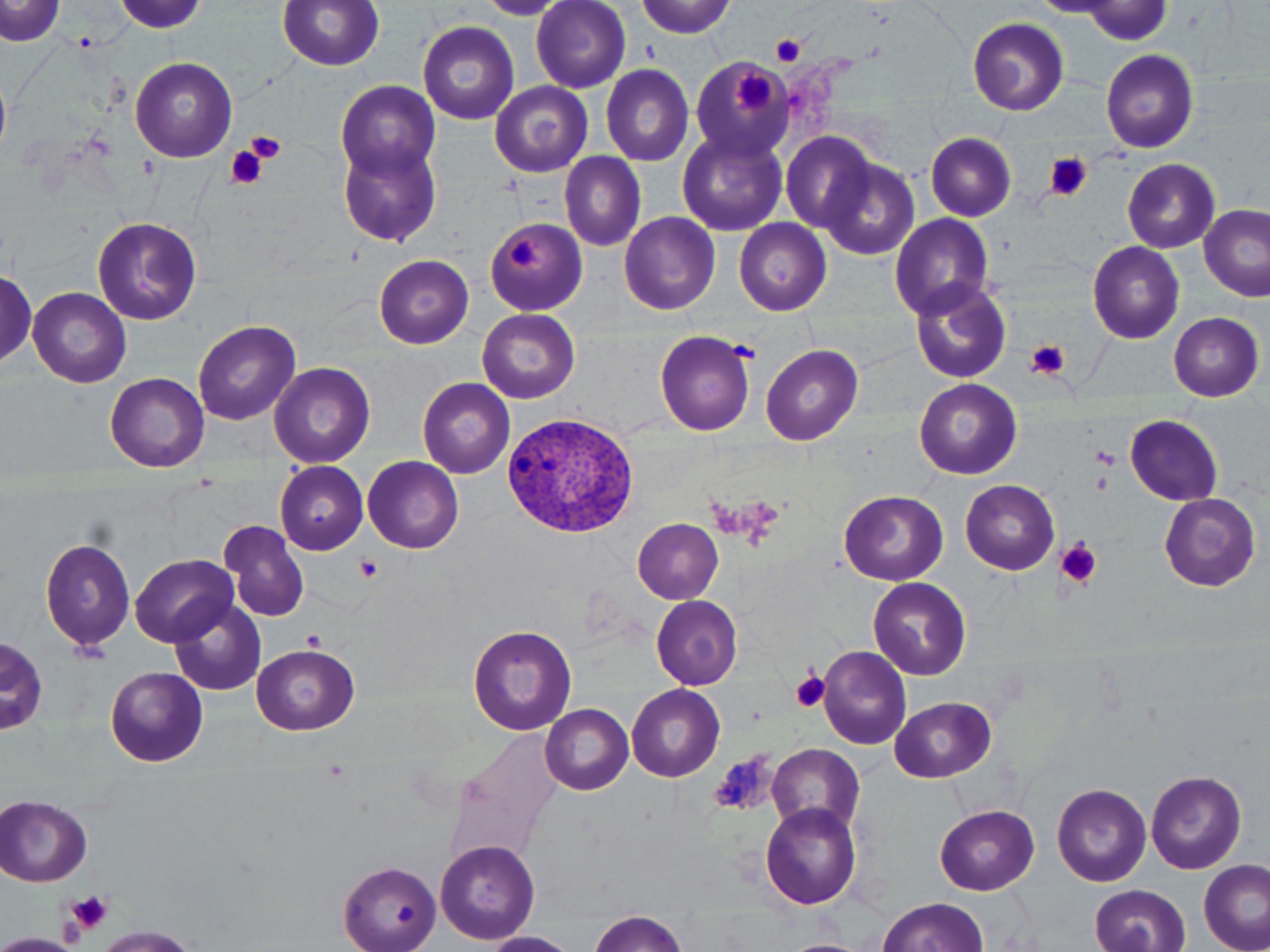
Summary:
  - Coordinate format: approximate bounding boxes as named x1/y1/x2/y2 corners in pixels
  - Platelet locations: (x1=1084, y1=1, x2=1171, y2=46), (x1=770, y1=35, x2=808, y2=68), (x1=732, y1=69, x2=773, y2=113), (x1=246, y1=132, x2=286, y2=162), (x1=226, y1=147, x2=266, y2=189), (x1=1042, y1=153, x2=1093, y2=202), (x1=509, y1=238, x2=542, y2=270), (x1=1025, y1=340, x2=1073, y2=380), (x1=1091, y1=448, x2=1119, y2=466), (x1=1056, y1=538, x2=1102, y2=587), (x1=354, y1=554, x2=383, y2=582), (x1=303, y1=631, x2=326, y2=650), (x1=791, y1=671, x2=831, y2=714), (x1=712, y1=752, x2=775, y2=817), (x1=67, y1=889, x2=112, y2=932)
  - Plasmodium vivax-infected red blood cell locations: (x1=501, y1=410, x2=644, y2=539)
  - Uninfected red blood cell locations: (x1=0, y1=0, x2=66, y2=46), (x1=278, y1=0, x2=384, y2=71), (x1=117, y1=1, x2=205, y2=32), (x1=533, y1=1, x2=631, y2=94), (x1=635, y1=1, x2=735, y2=37), (x1=1034, y1=2, x2=1114, y2=16), (x1=967, y1=17, x2=1069, y2=116), (x1=419, y1=21, x2=517, y2=124), (x1=1100, y1=49, x2=1199, y2=153), (x1=130, y1=56, x2=237, y2=162), (x1=687, y1=56, x2=790, y2=158), (x1=601, y1=65, x2=694, y2=166), (x1=0, y1=77, x2=11, y2=155), (x1=335, y1=81, x2=441, y2=185), (x1=490, y1=82, x2=591, y2=179), (x1=677, y1=128, x2=789, y2=236), (x1=781, y1=132, x2=877, y2=235), (x1=927, y1=133, x2=1016, y2=221), (x1=338, y1=142, x2=441, y2=245), (x1=561, y1=153, x2=646, y2=251), (x1=817, y1=158, x2=920, y2=260), (x1=1123, y1=159, x2=1219, y2=253), (x1=837, y1=174, x2=958, y2=282), (x1=1199, y1=205, x2=1269, y2=301), (x1=618, y1=212, x2=720, y2=314), (x1=890, y1=213, x2=994, y2=317), (x1=92, y1=216, x2=202, y2=325), (x1=485, y1=218, x2=586, y2=314), (x1=734, y1=218, x2=831, y2=316), (x1=1088, y1=241, x2=1185, y2=343), (x1=374, y1=255, x2=474, y2=348), (x1=0, y1=272, x2=39, y2=365), (x1=908, y1=277, x2=1012, y2=383), (x1=29, y1=287, x2=132, y2=388), (x1=478, y1=308, x2=580, y2=404), (x1=1168, y1=312, x2=1263, y2=401), (x1=194, y1=320, x2=299, y2=425), (x1=654, y1=329, x2=758, y2=435), (x1=762, y1=344, x2=863, y2=445), (x1=270, y1=362, x2=377, y2=468), (x1=105, y1=373, x2=208, y2=472), (x1=418, y1=377, x2=515, y2=477), (x1=915, y1=378, x2=1021, y2=478), (x1=1126, y1=414, x2=1222, y2=506), (x1=363, y1=456, x2=463, y2=553), (x1=275, y1=460, x2=368, y2=555), (x1=961, y1=479, x2=1060, y2=575), (x1=839, y1=490, x2=948, y2=585), (x1=1158, y1=492, x2=1260, y2=591), (x1=633, y1=518, x2=723, y2=603), (x1=217, y1=519, x2=310, y2=622), (x1=40, y1=537, x2=135, y2=652), (x1=132, y1=554, x2=237, y2=645), (x1=869, y1=577, x2=971, y2=679), (x1=650, y1=595, x2=744, y2=689), (x1=171, y1=599, x2=266, y2=696), (x1=468, y1=624, x2=577, y2=735), (x1=2, y1=638, x2=47, y2=735), (x1=252, y1=643, x2=359, y2=735), (x1=817, y1=644, x2=912, y2=751), (x1=106, y1=666, x2=208, y2=767), (x1=627, y1=684, x2=724, y2=783), (x1=891, y1=697, x2=997, y2=782), (x1=541, y1=704, x2=633, y2=794), (x1=447, y1=731, x2=564, y2=859), (x1=769, y1=747, x2=863, y2=832), (x1=1146, y1=771, x2=1248, y2=875), (x1=1053, y1=784, x2=1151, y2=886), (x1=0, y1=796, x2=92, y2=887), (x1=760, y1=803, x2=862, y2=912), (x1=935, y1=804, x2=1039, y2=894), (x1=436, y1=840, x2=540, y2=944), (x1=1200, y1=860, x2=1269, y2=952), (x1=339, y1=862, x2=442, y2=952), (x1=1091, y1=885, x2=1190, y2=952), (x1=877, y1=898, x2=988, y2=951), (x1=590, y1=910, x2=690, y2=951), (x1=91, y1=925, x2=197, y2=952), (x1=479, y1=933, x2=578, y2=952), (x1=785, y1=939, x2=863, y2=952)
  - Slide-level diagnosis: Plasmodium vivax
  - Image size: 1270×952 pixels
  - Preparation: thin blood film
  - Modality: optical microscopy
  - Magnification: 1000x
  - Field of view: one of a larger specimen
  - Stain: May-Grünwald-Giemsa